Name the parasite shown.
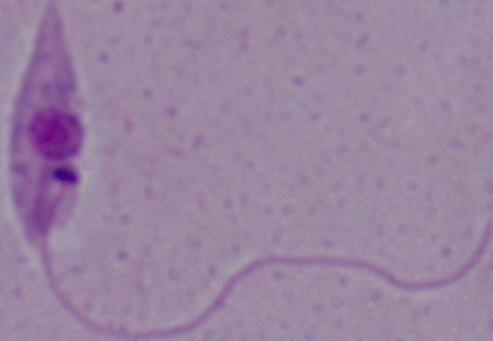
This is Leishmania.

magnification = 1000x
modality = micrograph